Report the malaria status of this cell.
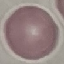
Uninfected.

capture = smartphone through the microscope eyepiece
stain = Giemsa
preparation = thin smear
image type = automatically extracted cell patch, resized to 64 × 64 pixels